Give the extent of all uninfected red blood cells.
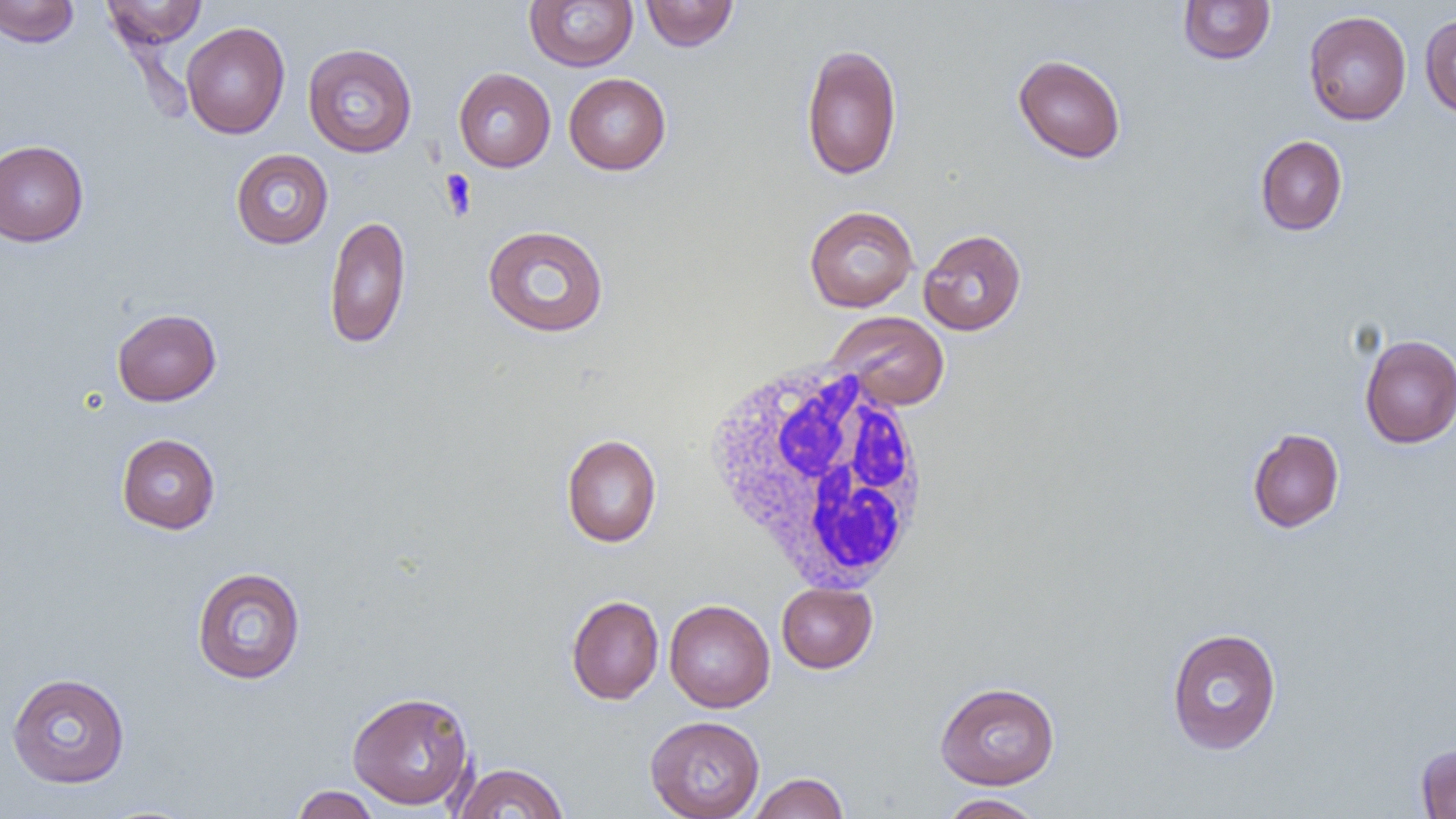
Approximate bounding boxes as (x1, y1, x2, y2) in pixels.
Uninfected red blood cells: (0, 0, 79, 48), (101, 0, 208, 50), (640, 0, 738, 51), (525, 1, 638, 71), (1177, 1, 1275, 65), (1303, 10, 1412, 125), (1419, 15, 1456, 118), (180, 22, 291, 139), (800, 42, 903, 180), (302, 43, 418, 157), (1013, 54, 1126, 163), (453, 67, 556, 172), (564, 73, 671, 175), (1255, 135, 1348, 236), (0, 140, 89, 247), (230, 149, 334, 249), (804, 205, 919, 312), (324, 215, 411, 349), (482, 225, 610, 337), (918, 229, 1027, 335), (112, 308, 222, 406), (827, 311, 950, 410), (1358, 335, 1456, 448), (1247, 428, 1344, 533), (116, 433, 220, 534), (561, 433, 662, 548), (190, 566, 307, 684), (776, 582, 877, 673), (566, 595, 664, 705), (664, 599, 775, 713), (1166, 627, 1282, 755), (6, 672, 130, 788), (934, 681, 1060, 789), (347, 690, 475, 811), (645, 715, 765, 819), (1415, 743, 1456, 818), (452, 763, 569, 818), (747, 773, 850, 818), (290, 785, 382, 819), (938, 793, 1045, 819).

{
  "slide_level_diagnosis": "negative for blood parasites",
  "modality": "light microscopy",
  "field_of_view": "one of a larger specimen",
  "preparation": "thin blood film",
  "image_size": "1456×819 pixels",
  "white_blood_cell_locations": "approximate bounding boxes as (x1, y1, x2, y2) in pixels: (700, 360, 937, 593)",
  "magnification": "1000x",
  "platelet_locations": "approximate bounding boxes as (x1, y1, x2, y2) in pixels: (440, 169, 478, 220)"
}